State which parasite is depicted.
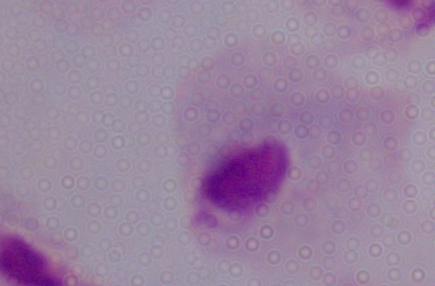
A trichomonad.

Photomicrograph. Captured at 1000x magnification.